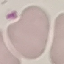

Summary:
  - Result: no malaria parasites seen
  - Image type: automatically extracted cell patch, resized to 64 × 64 pixels
  - Capture: smartphone camera at the microscope eyepiece
  - Stain: Giemsa
  - Preparation: thin blood smear